State the blood parasite species.
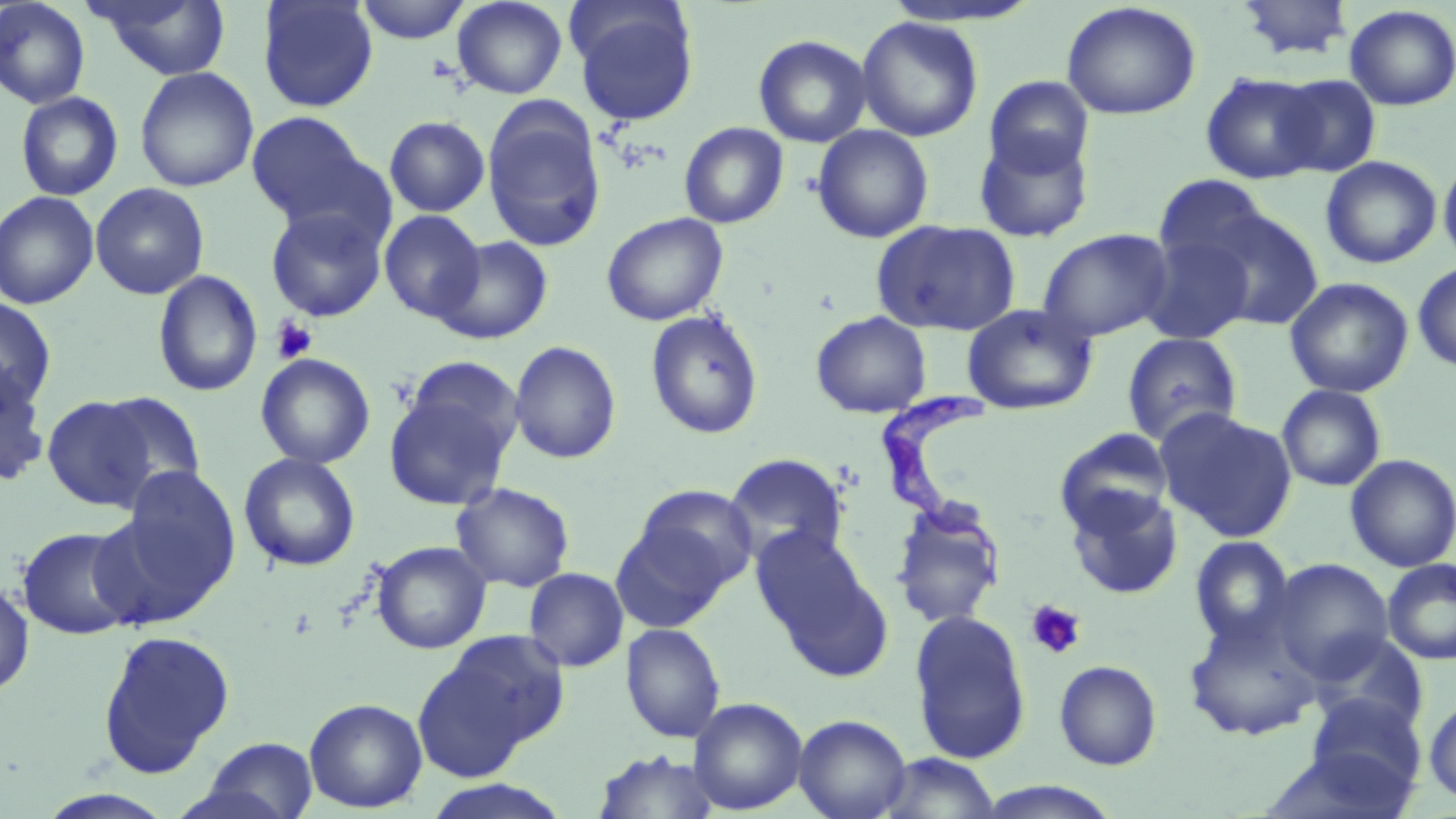

Trypanosoma brucei.

Approximate bounding boxes as (x1, y1, x2, y2) in pixels. Uninfected red blood cell locations: (89, 0, 233, 80), (257, 0, 378, 112), (355, 0, 472, 44), (452, 0, 568, 99), (1236, 0, 1354, 60), (0, 1, 91, 109), (1060, 1, 1201, 120), (570, 4, 700, 126), (1344, 4, 1456, 111), (856, 16, 984, 142), (753, 34, 873, 147), (134, 66, 259, 193), (1201, 72, 1325, 184), (1274, 74, 1382, 177), (984, 76, 1094, 178), (15, 92, 123, 201), (482, 104, 606, 252), (246, 111, 372, 226), (384, 116, 490, 217), (679, 122, 789, 229), (811, 125, 934, 243), (972, 129, 1095, 244), (1438, 153, 1456, 268), (1320, 155, 1442, 269), (1151, 174, 1273, 279), (90, 182, 210, 300), (0, 190, 100, 309), (265, 206, 388, 322), (1197, 206, 1324, 330), (379, 210, 486, 323), (601, 212, 728, 326), (871, 219, 1021, 336), (1037, 228, 1174, 342), (1139, 232, 1255, 345), (435, 236, 553, 344), (1412, 262, 1456, 372), (152, 270, 262, 398), (1284, 277, 1414, 398), (0, 297, 57, 412), (961, 303, 1099, 415), (645, 310, 765, 440), (810, 311, 932, 418), (1121, 331, 1242, 446), (509, 341, 622, 464), (255, 353, 375, 469), (0, 362, 51, 487), (383, 377, 520, 511), (1277, 384, 1387, 492), (94, 391, 208, 500), (43, 398, 158, 513), (1155, 407, 1300, 542), (1054, 427, 1175, 536), (238, 453, 361, 572), (723, 453, 849, 565), (1344, 454, 1456, 573), (113, 465, 242, 603), (451, 482, 575, 592), (630, 484, 757, 593), (1063, 484, 1183, 600), (889, 500, 1007, 629), (611, 518, 737, 633), (17, 525, 139, 640), (750, 526, 892, 680), (1190, 536, 1295, 650), (371, 540, 491, 654), (1268, 558, 1394, 681), (1382, 558, 1456, 665), (523, 567, 629, 672), (0, 579, 35, 697), (908, 608, 1032, 765), (1182, 610, 1323, 742), (621, 623, 727, 743), (97, 628, 235, 779), (415, 630, 567, 777), (1307, 632, 1429, 738), (1054, 660, 1162, 770), (1306, 696, 1426, 798), (1423, 696, 1456, 804), (304, 697, 427, 813), (687, 697, 808, 815), (793, 713, 912, 819), (194, 736, 319, 819), (1266, 746, 1417, 819), (591, 749, 724, 819), (875, 752, 1002, 818), (417, 778, 576, 819), (971, 780, 1127, 818). Trypanosoma brucei locations: (881, 379, 1004, 588). Platelet locations: (270, 317, 317, 364), (1025, 599, 1087, 660). Light microscopy. Single field of view. Image is 1456×819 pixels. Thin blood film. Captured at 1000x magnification. May-Grünwald-Giemsa-stained preparation.